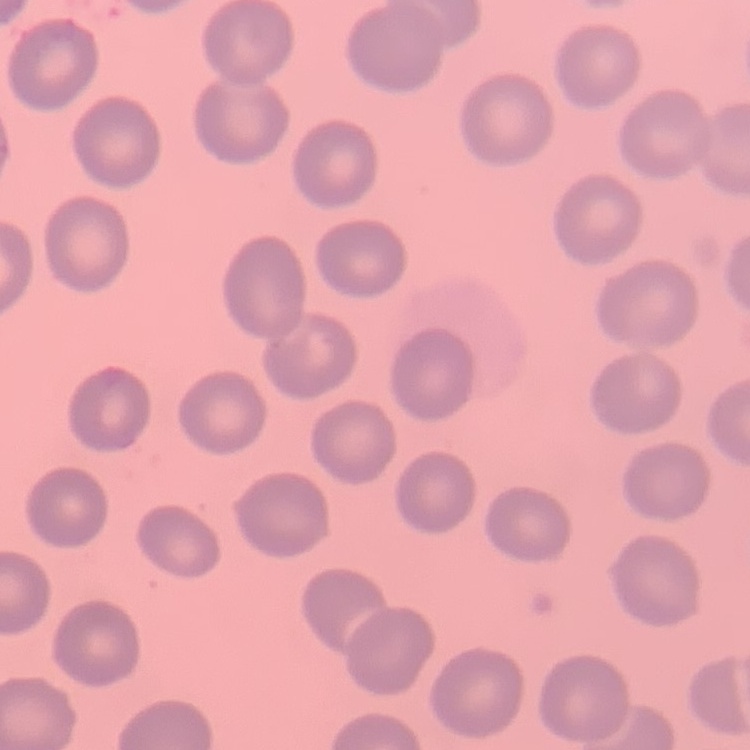
erythrocyte morphology = no rouleaux formation
preparation = thin peripheral smear
image type = square crop of a larger photomicrograph
stain = Field's or Giemsa